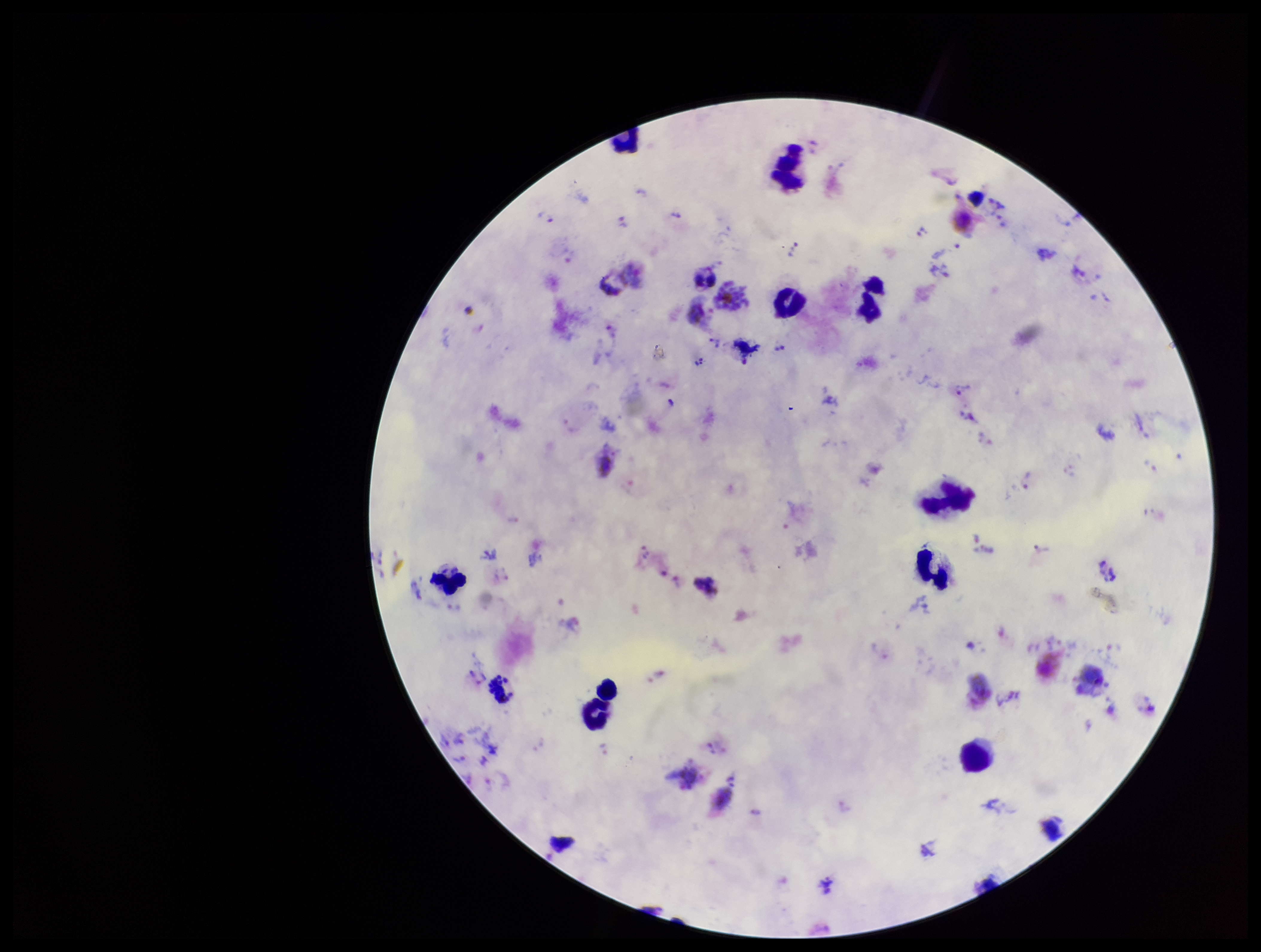

Summary:
  - Parasite count: 17
  - Field of view: single
  - Plasmodium parasites: seen
  - Leukocyte count: 11
  - Stain: Giemsa
  - Preparation: thick
  - Image size: 1261×952 pixels
  - Patient malaria status: positive
  - Species reported for this patient: Plasmodium vivax
  - Capture: smartphone photograph through the microscope eyepiece